Identify the cell.
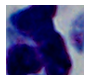
A leukocyte.

magnification = 1000x
modality = photomicrograph